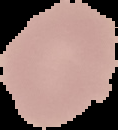
The area outside the segmented cell region is set to black. Result: negative for Plasmodium parasites. From a thin blood film. Image is 118×130 pixels.